Point out each Plasmodium parasite.
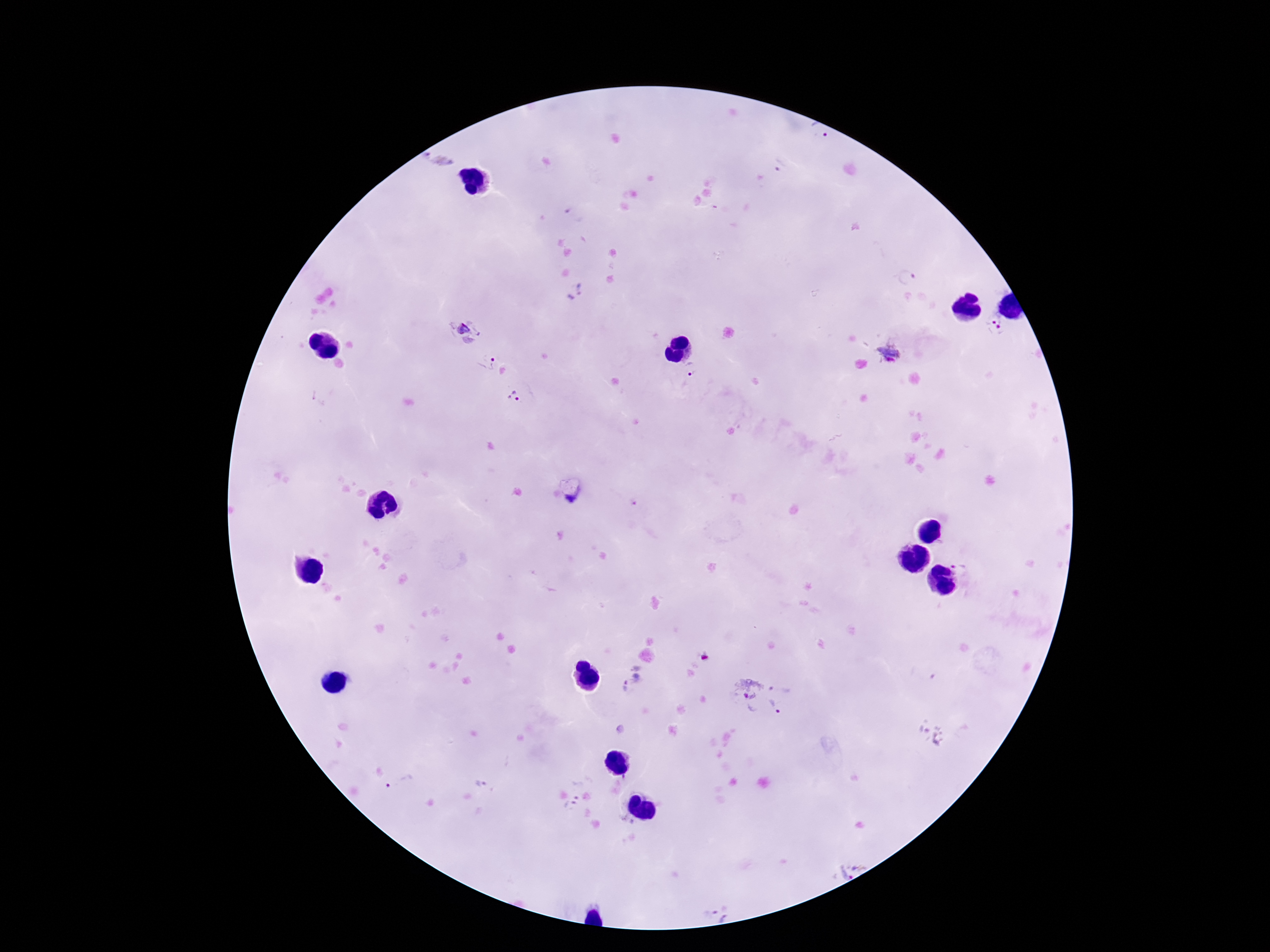
Approximate centers as [x, y] in pixels.
Plasmodium parasites: [818, 134], [780, 164], [907, 277], [575, 292], [995, 326], [465, 331], [890, 353], [487, 360], [692, 370], [515, 397], [631, 677], [782, 685], [745, 697], [775, 710], [482, 782], [399, 783], [576, 789], [570, 806], [850, 869], [718, 914].

Summary:
  - Image size: 1270×952 pixels
  - Patient malaria status: positive
  - Magnification: 100x
  - Field of view: one from this slide
  - Capture: smartphone camera through the microscope eyepiece
  - Preparation: thick blood film
  - Stain: Giemsa